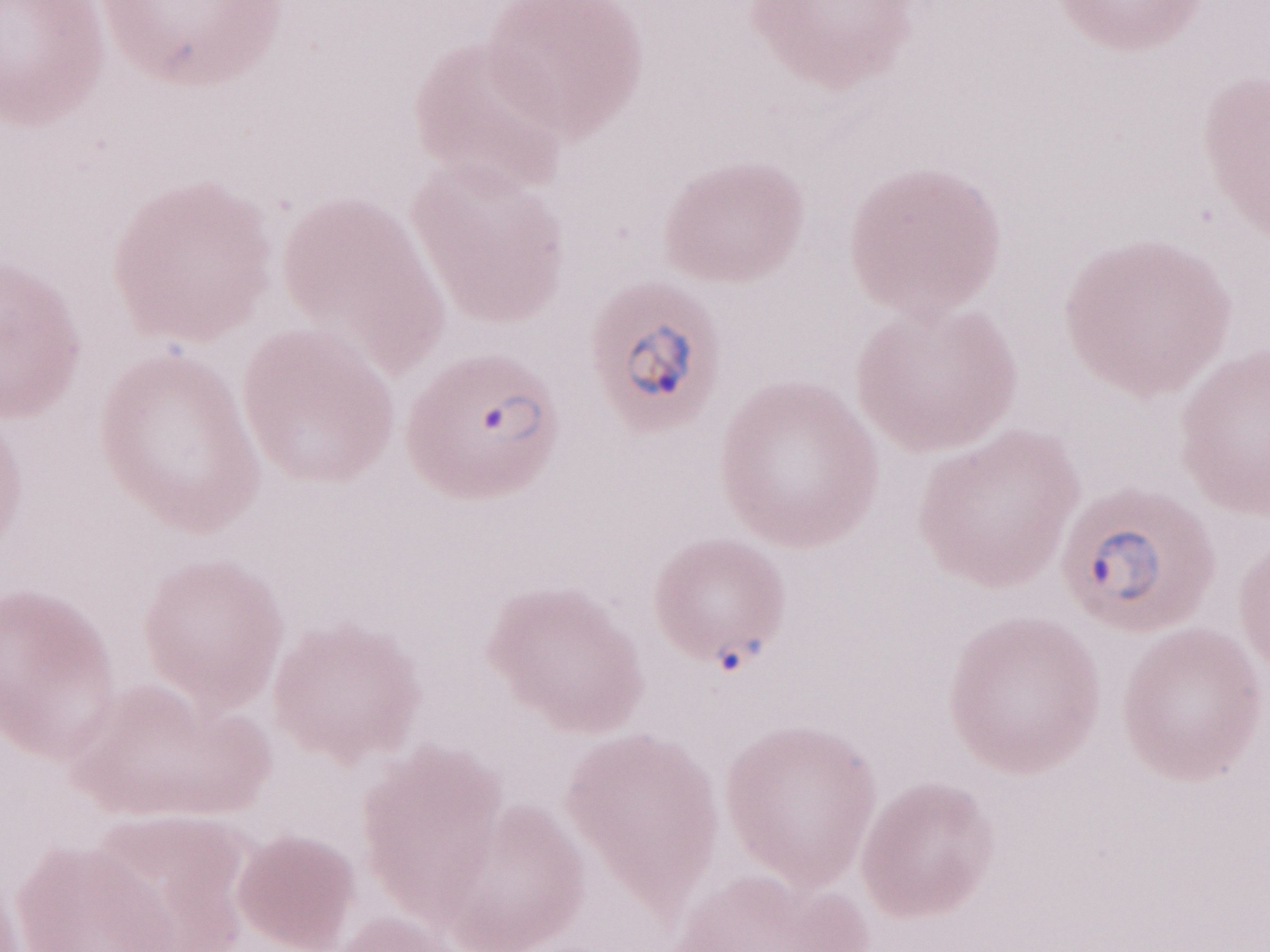 Olympus BX43 microscope, Olympus DP73 camera. One field of this slide. Thin blood smear. Image is 1270×952 pixels. Malaria diagnosis (patient-level): positive. 1,000x magnification. May-Grünwald-Giemsa (MGG) stain.